Report the malaria status of this cell.
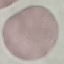
It is uninfected.

Photographed with a smartphone camera at the microscope eyepiece. Thin blood smear. Automatically extracted cell patch, resized to 64 × 64 pixels. Giemsa-stained preparation.